Report the malaria status of this cell.
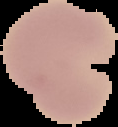

It is uninfected.

preparation = thin blood smear
image size = 118×127 pixels
image type = cell region segmented out of the field of view; surrounding area masked to black